Identify the blood parasite species.
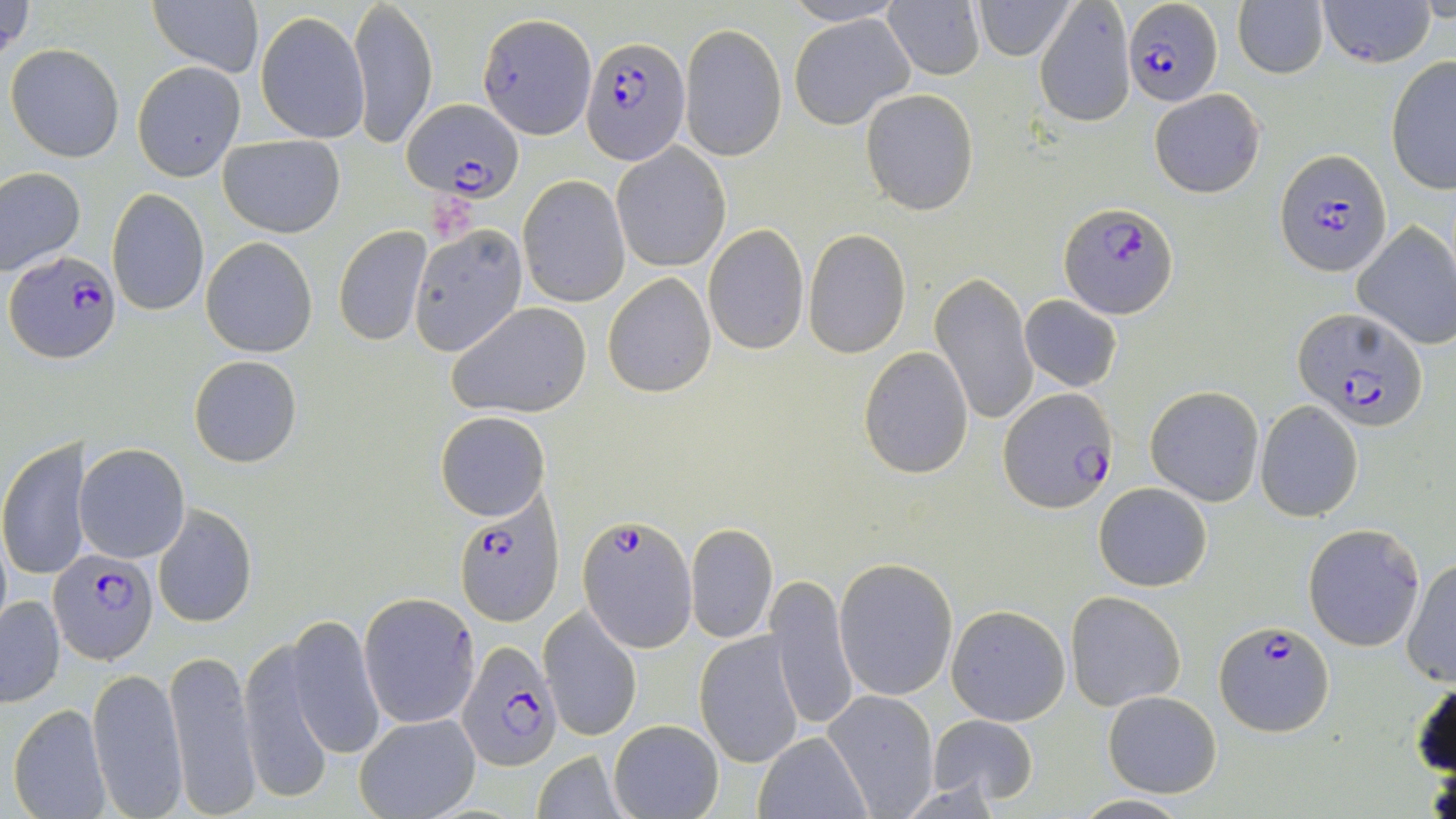

Plasmodium falciparum.

Approximate bounding boxes as (x1,y1)-(x2,y2) corner pairs in pixels. Plasmodium falciparum-infected red blood cell locations: (1124,0)-(1223,106), (478,13)-(594,136), (583,35)-(691,165), (403,98)-(525,201), (1276,148)-(1390,276), (1060,201)-(1178,319), (5,252)-(121,363), (1294,308)-(1430,432), (999,389)-(1119,513), (451,501)-(564,624), (579,512)-(697,649), (48,549)-(158,663), (1213,620)-(1336,736), (449,640)-(559,771). Uninfected red blood cell locations: (1,0)-(35,65), (349,0)-(438,152), (973,0)-(1076,59), (1033,0)-(1136,126), (1232,0)-(1329,78), (1318,0)-(1436,68), (147,2)-(263,78), (777,2)-(913,26), (884,2)-(985,79), (255,12)-(369,144), (789,12)-(915,130), (679,23)-(787,162), (5,43)-(126,163), (802,52)-(939,184), (1385,55)-(1456,196), (133,61)-(244,180), (1149,88)-(1266,198), (861,89)-(978,215), (218,135)-(345,238), (612,143)-(730,272), (0,166)-(85,277), (518,175)-(629,306), (107,188)-(209,316), (1352,221)-(1456,351), (408,223)-(528,355), (702,223)-(809,355), (333,225)-(431,347), (803,228)-(911,359), (201,237)-(317,357), (603,272)-(715,397), (930,273)-(1039,426), (1019,295)-(1122,391), (447,302)-(592,419), (858,347)-(975,479), (189,355)-(303,468), (1145,385)-(1265,505), (1254,400)-(1365,522), (435,411)-(550,521), (0,436)-(88,584), (75,443)-(189,562), (1094,483)-(1212,591), (153,506)-(258,628), (1301,522)-(1426,651), (686,523)-(778,642), (834,557)-(958,702), (1401,557)-(1456,686), (768,575)-(858,735), (1064,590)-(1187,712), (360,592)-(480,728), (1,596)-(65,707), (946,604)-(1072,725), (540,607)-(642,742), (282,615)-(385,762), (695,630)-(805,768), (239,634)-(350,802), (162,644)-(261,818), (87,667)-(187,817), (1410,677)-(1455,776), (823,690)-(939,817), (1102,690)-(1222,797), (8,703)-(111,819), (927,713)-(1038,805), (355,714)-(480,819), (608,718)-(724,819), (754,731)-(871,818), (532,752)-(630,818), (1071,794)-(1191,818). Single field of view. Image is 1456×819 pixels. 1000x magnification. Thin blood smear. May-Grünwald-Giemsa-stained preparation. Optical microscopy.